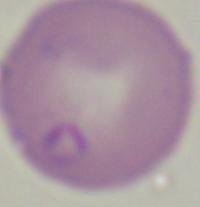

identification: Babesia
modality: micrograph
magnification: 1000x